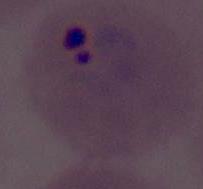
Summary:
  - Magnification: 400x or 1000x
  - Identification: Plasmodium
  - Modality: photomicrograph